Point out Plasmodium parasites and leukocytes.
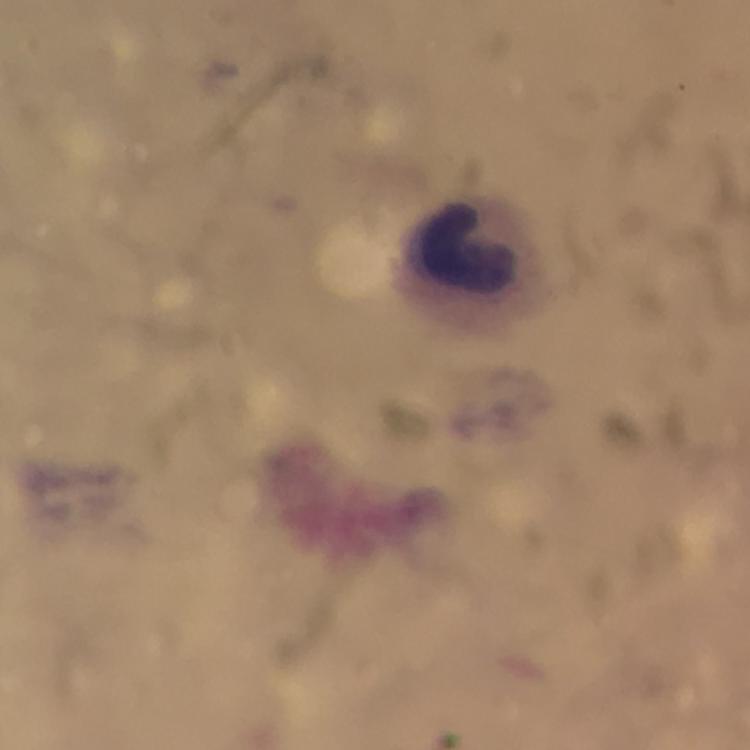

No Plasmodium parasites detected.
Approximate centers as (x, y) in pixels.
Leukocytes: (467, 250).

context = from a diagnostic examination for malaria
immersion oil = used
image size = 750×750 pixels
magnification = 100x
stain = Giemsa
preparation = thick smear
cropped from = a single field of view
capture = smartphone photograph through a microscope